Describe the morphology of the red blood cells.
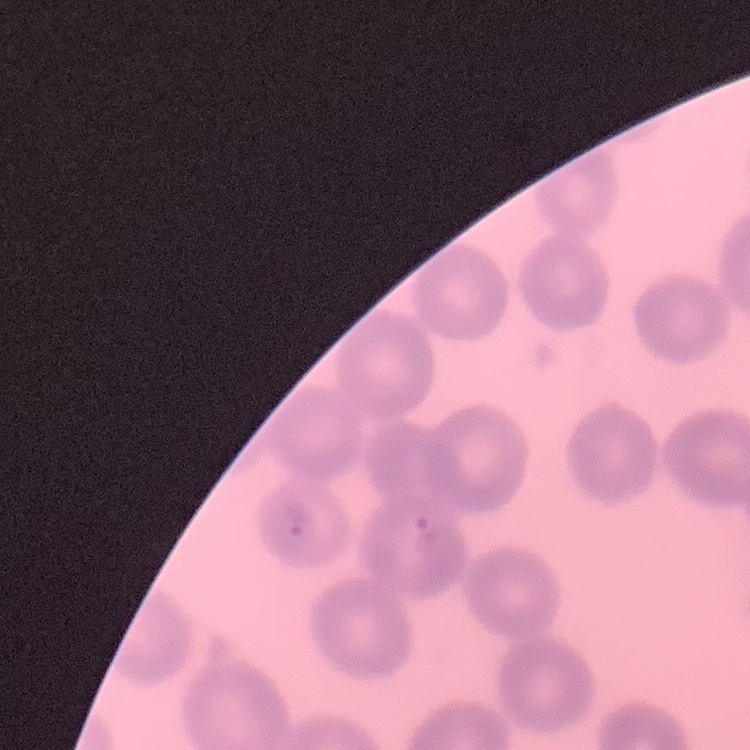
They show no rouleaux formation.

Summary:
  - Image type: square crop of a larger photomicrograph
  - Stain: Field's or Giemsa
  - Preparation: thin peripheral smear